Assess this cell for malaria.
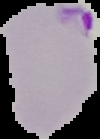

It is parasitized.

image_type: cell region segmented out of the field of view; surrounding area masked to black
image_size: 100×139 pixels
preparation: thin blood smear